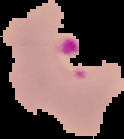

Summary:
  - Malaria status: parasitized
  - Image type: segmented cell region with the area outside set to black
  - Image size: 124×139 pixels
  - Preparation: thin blood smear